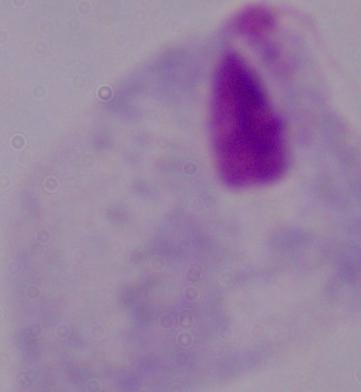

modality = micrograph
magnification = 1000x
identification = trichomonad